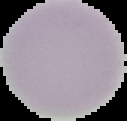
Summary:
  - Preparation: thin blood smear
  - Image type: cell region segmented out of the field of view; surrounding area masked to black
  - Image size: 127×121 pixels
  - Result: negative for Plasmodium parasites